Evaluate for parasitized red blood cells.
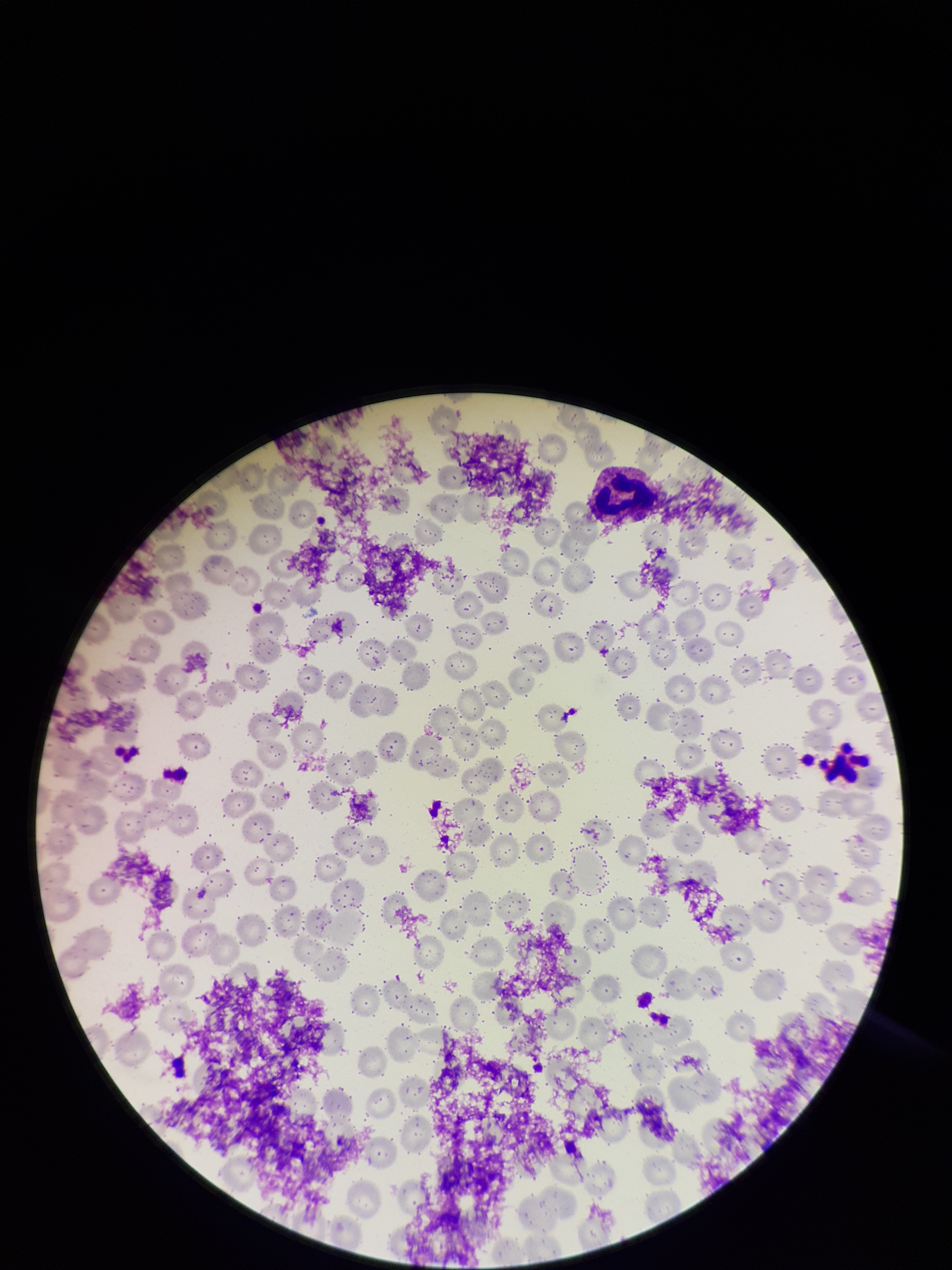

None identified.

One field from this slide. Image is 952×1270 pixels. Smartphone photograph taken through the eyepiece of a microscope. Patient malaria status: negative. Red blood cell count: 204. Parasitized red blood cell count: 0. Preparation: thin smear. Giemsa stain.